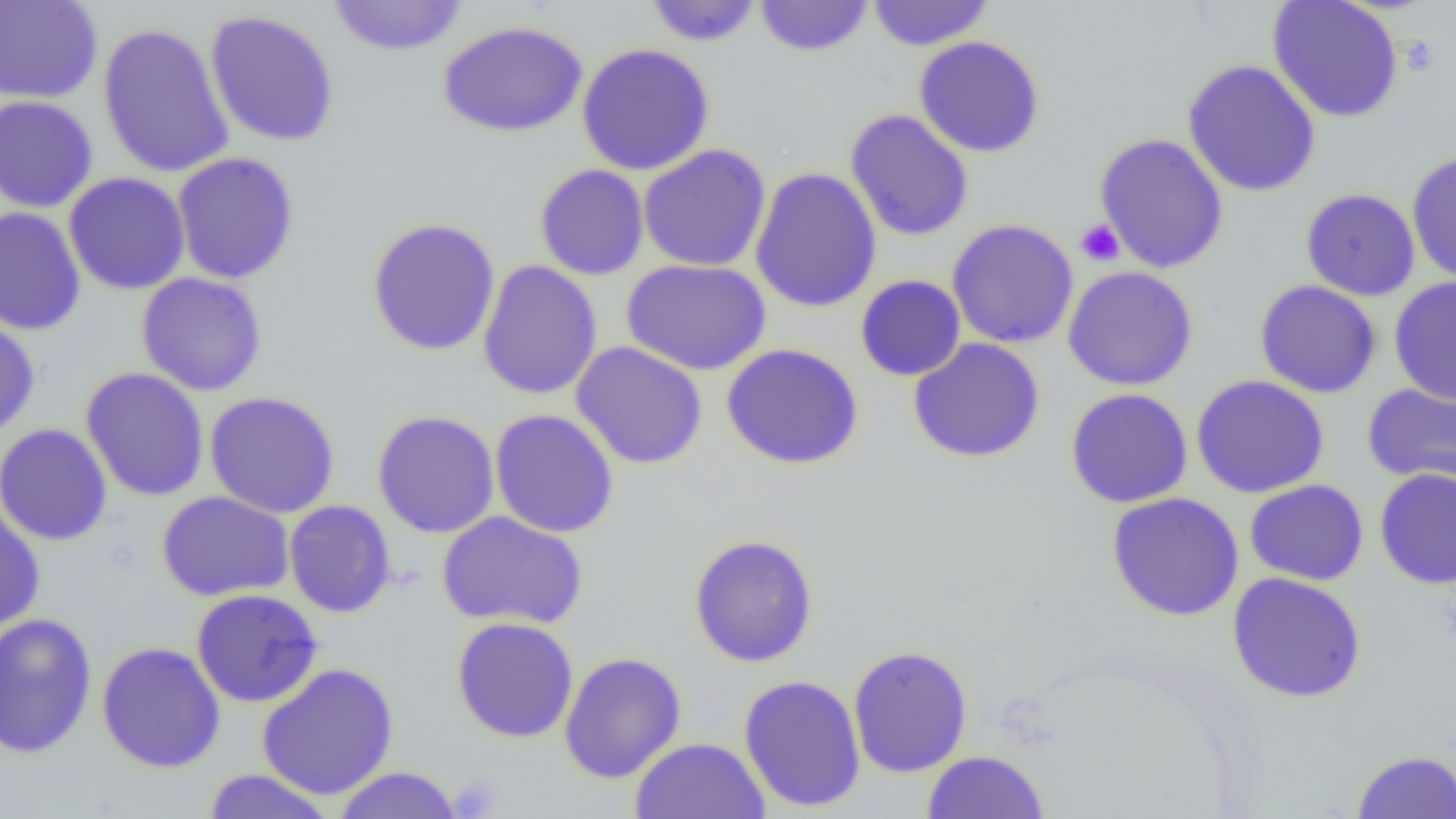
slide-level diagnosis = no evidence of blood parasites
preparation = thin blood film
field of view = single
modality = optical microscopy
magnification = 1000x
platelet locations = approximate bounding boxes as (x1,y1)-(x2,y2) corner pairs in pixels: (1398,34)-(1442,78), (1075,220)-(1125,267), (446,773)-(502,818)
uninfected red blood cell locations = approximate bounding boxes as (x1,y1)-(x2,y2) corner pairs in pixels: (0,0)-(103,104), (327,0)-(469,56), (644,0)-(763,46), (755,0)-(873,57), (866,0)-(995,51), (1267,0)-(1404,123), (203,9)-(340,148), (438,20)-(588,137), (97,22)-(235,179), (913,36)-(1046,158), (576,43)-(715,175), (1182,60)-(1321,198), (0,96)-(99,213), (845,109)-(974,242), (1094,132)-(1229,274), (638,144)-(772,272), (1406,151)-(1456,286), (171,152)-(300,284), (534,163)-(649,281), (749,166)-(882,313), (63,172)-(190,295), (1300,188)-(1420,301), (0,207)-(85,336), (366,217)-(501,356), (947,218)-(1079,349), (620,258)-(772,376), (477,260)-(603,400), (1063,265)-(1199,391), (135,272)-(268,396), (855,275)-(966,381), (1389,276)-(1456,406), (1254,280)-(1381,398), (0,314)-(40,440), (907,338)-(1045,464), (571,341)-(708,469), (721,342)-(864,470), (80,367)-(210,502), (1190,375)-(1330,498), (1362,382)-(1456,489), (1064,388)-(1193,508), (203,391)-(340,518), (489,409)-(619,538), (372,410)-(500,539), (0,423)-(113,546), (1374,468)-(1456,590), (1244,479)-(1369,586), (156,491)-(294,602), (1105,491)-(1244,621), (284,500)-(396,618), (0,502)-(45,633), (436,511)-(588,630), (688,534)-(819,668), (1226,572)-(1367,703), (191,588)-(324,708), (0,612)-(98,759), (450,617)-(579,743), (97,641)-(226,773), (847,645)-(973,777), (559,652)-(686,784), (257,662)-(399,801), (738,674)-(866,812), (629,737)-(769,819), (1351,749)-(1456,818), (921,750)-(1049,818), (331,767)-(464,818), (202,768)-(337,819)
image size = 1456×819 pixels